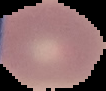
Malaria status: uninfected. From a thin blood smear. Segmented cell region on a black background. Image is 106×91 pixels.